Give the extent of all uninfected red blood cells.
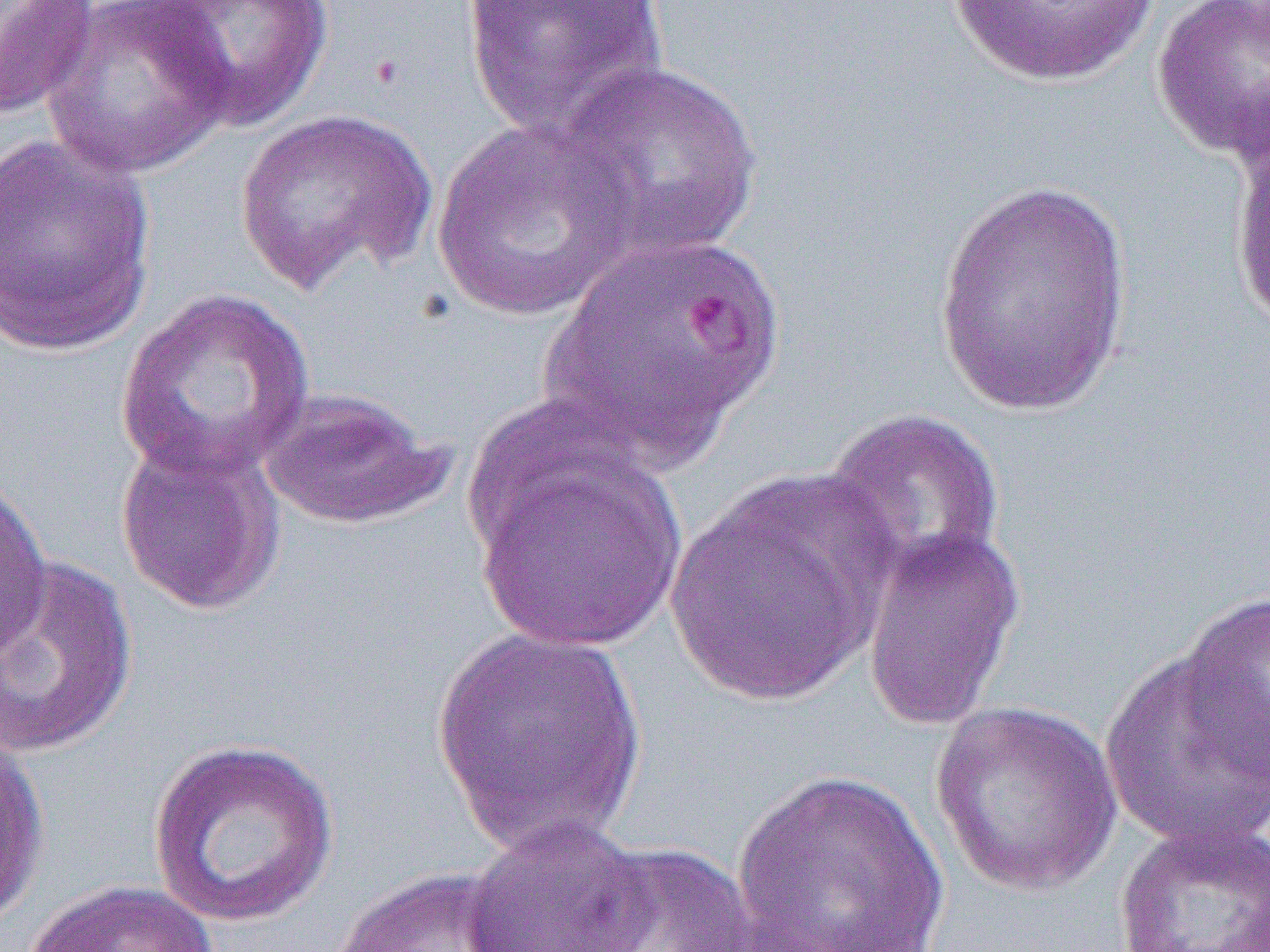

Approximate bounding boxes as named x1/y1/x2/y2 corners in pixels.
Uninfected red blood cells: (x1=145, y1=0, x2=335, y2=132), (x1=459, y1=0, x2=670, y2=138), (x1=942, y1=0, x2=1163, y2=88), (x1=1151, y1=0, x2=1270, y2=162), (x1=0, y1=1, x2=100, y2=120), (x1=42, y1=1, x2=235, y2=179), (x1=553, y1=58, x2=766, y2=264), (x1=235, y1=108, x2=438, y2=295), (x1=430, y1=116, x2=640, y2=323), (x1=1229, y1=123, x2=1270, y2=345), (x1=0, y1=130, x2=157, y2=357), (x1=933, y1=177, x2=1136, y2=417), (x1=535, y1=231, x2=786, y2=470), (x1=114, y1=287, x2=316, y2=484), (x1=257, y1=387, x2=452, y2=530), (x1=820, y1=407, x2=1007, y2=591), (x1=114, y1=435, x2=285, y2=616), (x1=474, y1=446, x2=687, y2=655), (x1=664, y1=469, x2=895, y2=708), (x1=0, y1=471, x2=51, y2=664), (x1=861, y1=525, x2=1025, y2=732), (x1=1, y1=555, x2=139, y2=760), (x1=1177, y1=592, x2=1270, y2=786), (x1=430, y1=629, x2=652, y2=858), (x1=1099, y1=650, x2=1270, y2=853), (x1=929, y1=701, x2=1123, y2=898), (x1=0, y1=728, x2=50, y2=930), (x1=147, y1=736, x2=341, y2=928), (x1=730, y1=768, x2=952, y2=952), (x1=461, y1=815, x2=653, y2=952), (x1=1113, y1=820, x2=1269, y2=952), (x1=576, y1=841, x2=760, y2=952), (x1=332, y1=865, x2=527, y2=951), (x1=23, y1=879, x2=221, y2=952).

Slide-level diagnosis: Plasmodium falciparum. Captured at 1000x magnification. Optical microscopy. One field of a larger specimen. Thin blood smear. Image is 1270×952 pixels.